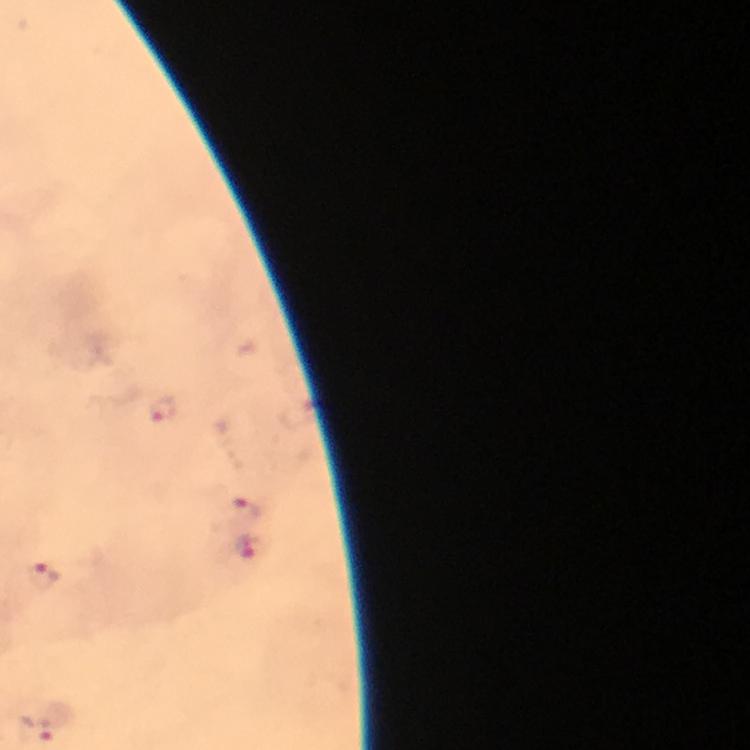

{
  "magnification": "100x",
  "immersion_oil": "used",
  "image_size": "750×750 pixels",
  "cropped_from": "one field of view",
  "capture": "smartphone camera through the microscope",
  "context": "from a malaria diagnostic workup",
  "plasmodium_parasite_locations": "approximate centers as [x, y] in pixels: [161, 409], [244, 510], [248, 549], [40, 575], [40, 728]",
  "preparation": "thick blood smear",
  "stain": "Giemsa"
}